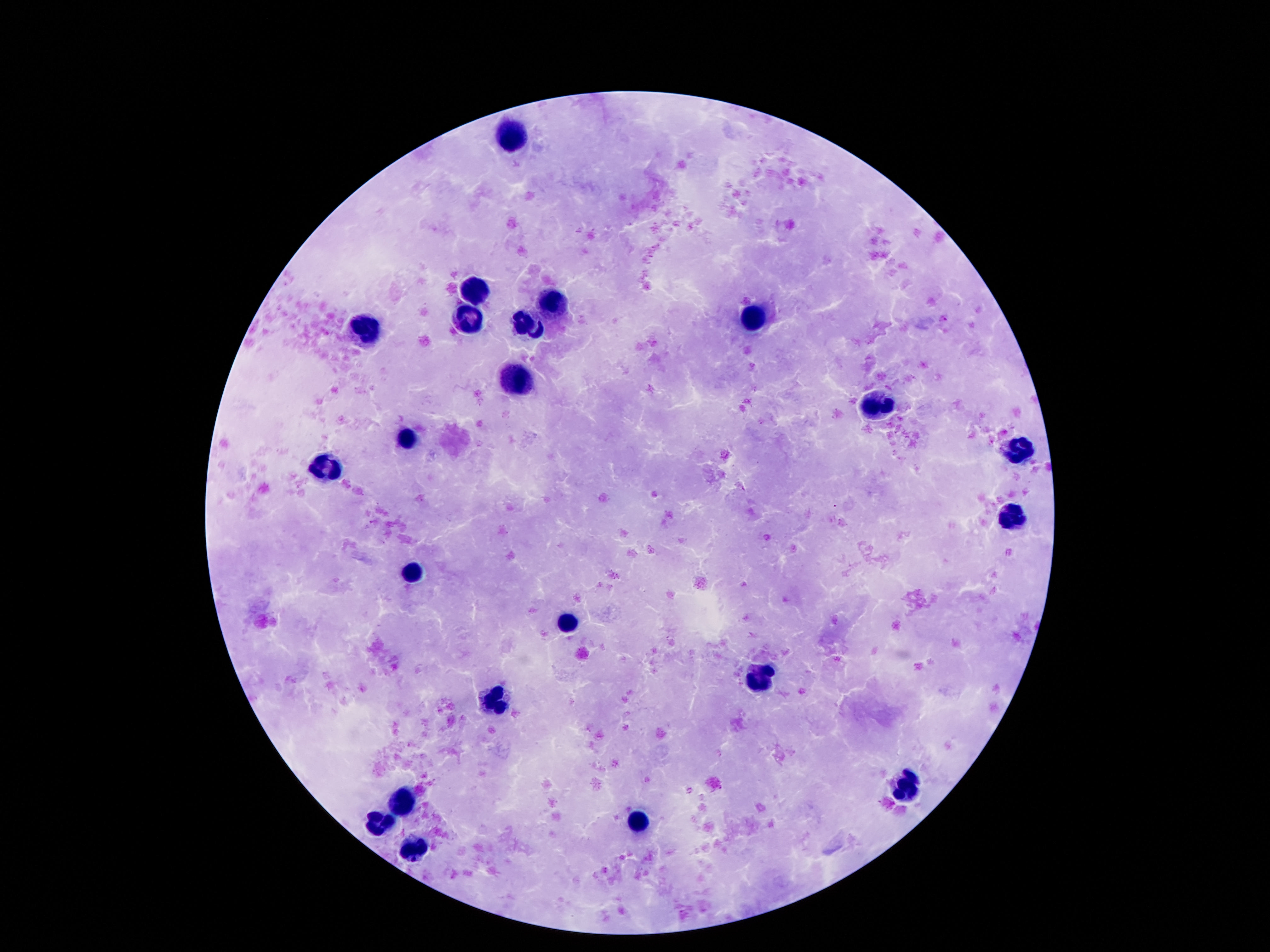
patient malaria status = negative
leukocyte locations = approximate centers as [x, y] in pixels: [511, 135], [475, 288], [555, 303], [756, 319], [531, 320], [466, 323], [365, 331], [519, 380], [880, 402], [407, 438], [1017, 453], [325, 469], [1012, 518], [413, 571], [566, 619], [763, 677], [495, 701], [904, 786], [400, 798], [641, 821], [380, 823], [416, 852]
field of view = one from this slide
stain = Giemsa
image size = 1270×952 pixels
magnification = 100x
preparation = thick blood smear
capture = smartphone camera through the microscope eyepiece